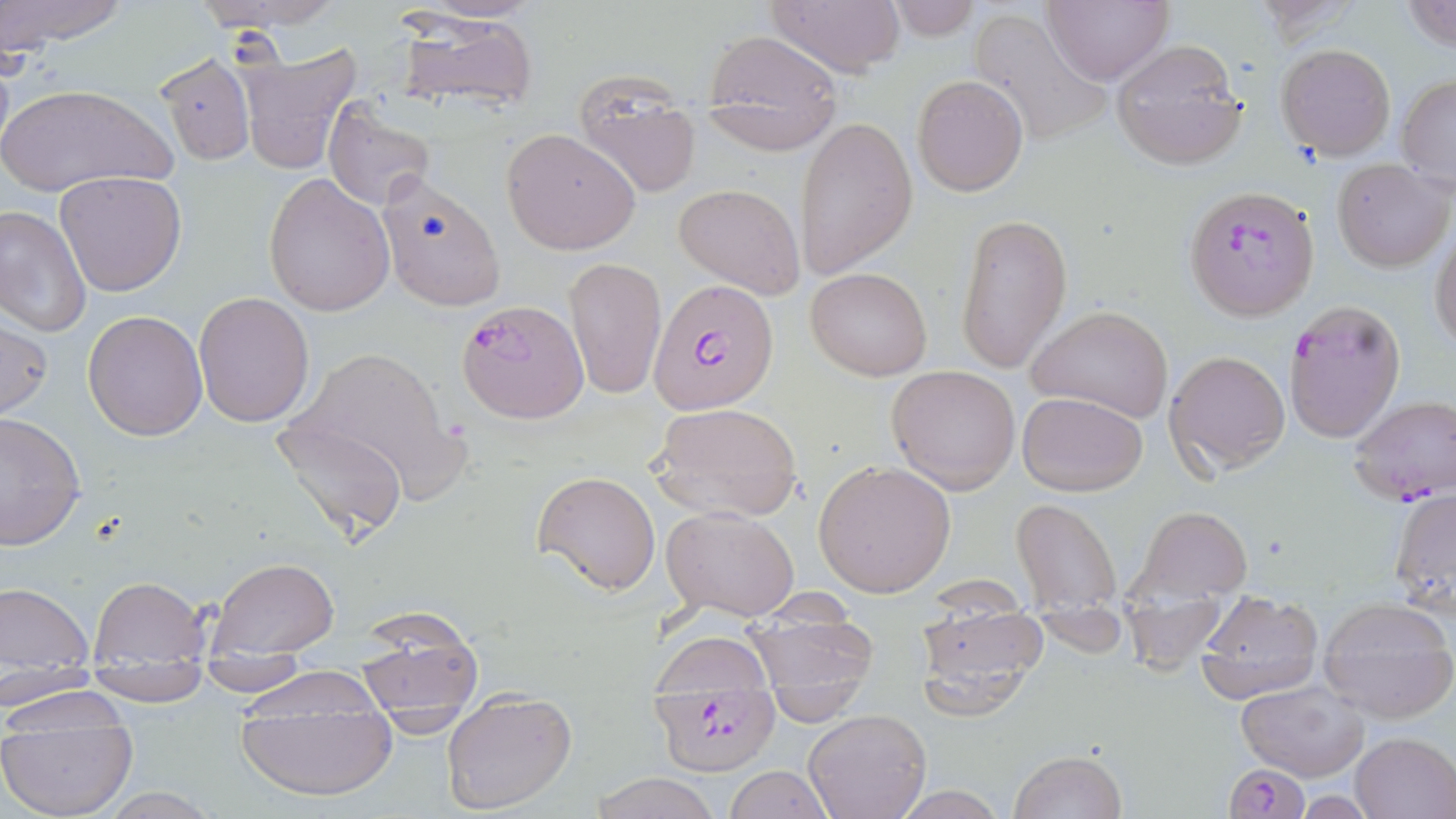

Approximate bounding boxes as [x1, y1, x2, y2] in pixels. Uninfected red blood cell locations: [0, 0, 130, 49], [192, 0, 342, 34], [764, 0, 906, 78], [883, 0, 982, 45], [1043, 0, 1171, 85], [1401, 0, 1456, 54], [968, 7, 1113, 148], [390, 10, 539, 116], [701, 25, 844, 144], [1110, 39, 1249, 170], [1276, 43, 1397, 161], [235, 45, 362, 174], [156, 52, 254, 165], [573, 71, 702, 198], [1397, 74, 1456, 190], [913, 75, 1030, 195], [2, 83, 177, 197], [322, 99, 437, 210], [795, 116, 917, 282], [502, 128, 641, 255], [1331, 159, 1453, 272], [55, 170, 185, 296], [374, 172, 506, 311], [264, 173, 394, 317], [674, 181, 804, 299], [0, 205, 92, 337], [954, 212, 1071, 374], [1430, 228, 1456, 351], [563, 255, 666, 400], [806, 267, 931, 379], [193, 291, 315, 428], [1027, 306, 1173, 424], [83, 310, 207, 439], [0, 315, 51, 420], [283, 344, 465, 497], [1164, 350, 1292, 475], [886, 365, 1021, 494], [1017, 390, 1148, 494], [648, 401, 805, 523], [0, 412, 86, 549], [271, 413, 409, 544], [813, 460, 956, 597], [532, 469, 661, 596], [1388, 486, 1455, 617], [1010, 497, 1122, 612], [662, 504, 801, 620], [1133, 505, 1253, 603], [205, 558, 339, 653], [88, 576, 211, 662], [0, 580, 96, 669], [1197, 591, 1324, 705], [1318, 597, 1456, 723], [913, 603, 1047, 722], [737, 605, 881, 703], [352, 611, 485, 728], [651, 632, 776, 694], [192, 656, 316, 699], [83, 664, 212, 706], [228, 666, 390, 719], [0, 667, 102, 708], [232, 672, 400, 766], [0, 676, 128, 730], [1235, 679, 1368, 782], [441, 688, 578, 815], [234, 708, 400, 805], [802, 709, 931, 819], [0, 723, 139, 819], [1350, 731, 1455, 817], [1008, 749, 1128, 819], [724, 765, 833, 819], [586, 773, 725, 819], [887, 785, 1011, 818], [87, 788, 226, 818]. Plasmodium falciparum-infected red blood cell locations: [1184, 186, 1319, 321], [651, 280, 779, 412], [457, 299, 589, 424], [1283, 299, 1406, 446], [1347, 395, 1456, 505], [649, 689, 780, 777], [1222, 764, 1312, 819]. Slide-level diagnosis: Plasmodium falciparum. May-Grünwald-Giemsa-stained preparation. Thin blood film. 1000x magnification. Image is 1456×819 pixels. Single field of view. Light microscopy.